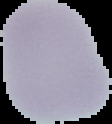
result = no malaria parasites seen
image type = segmented cell region with the area outside set to black
preparation = thin blood smear
image size = 112×124 pixels